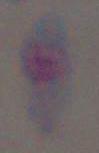
Summary:
  - Identification: Toxoplasma gondii
  - Magnification: 1000x
  - Modality: micrograph